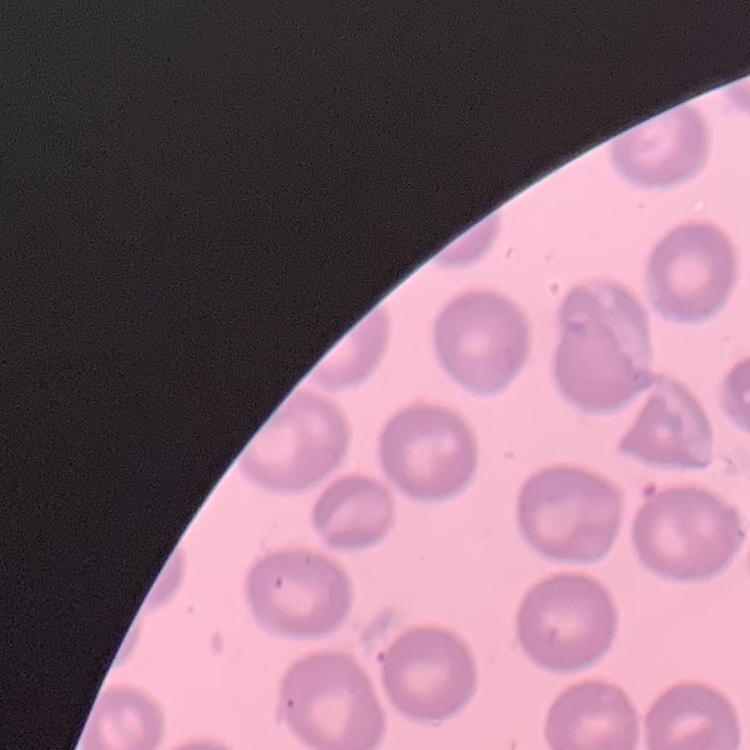

erythrocyte morphology = no rouleaux formation
image type = one tile cut from a larger photomicrograph
stain = Field's or Giemsa
preparation = thin blood smear